State which parasite is depicted.
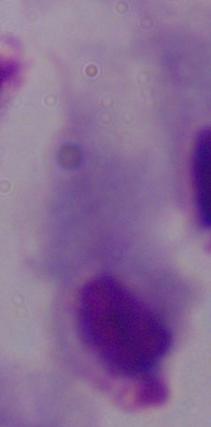

This is a trichomonad.

modality = photomicrograph
magnification = 1000x